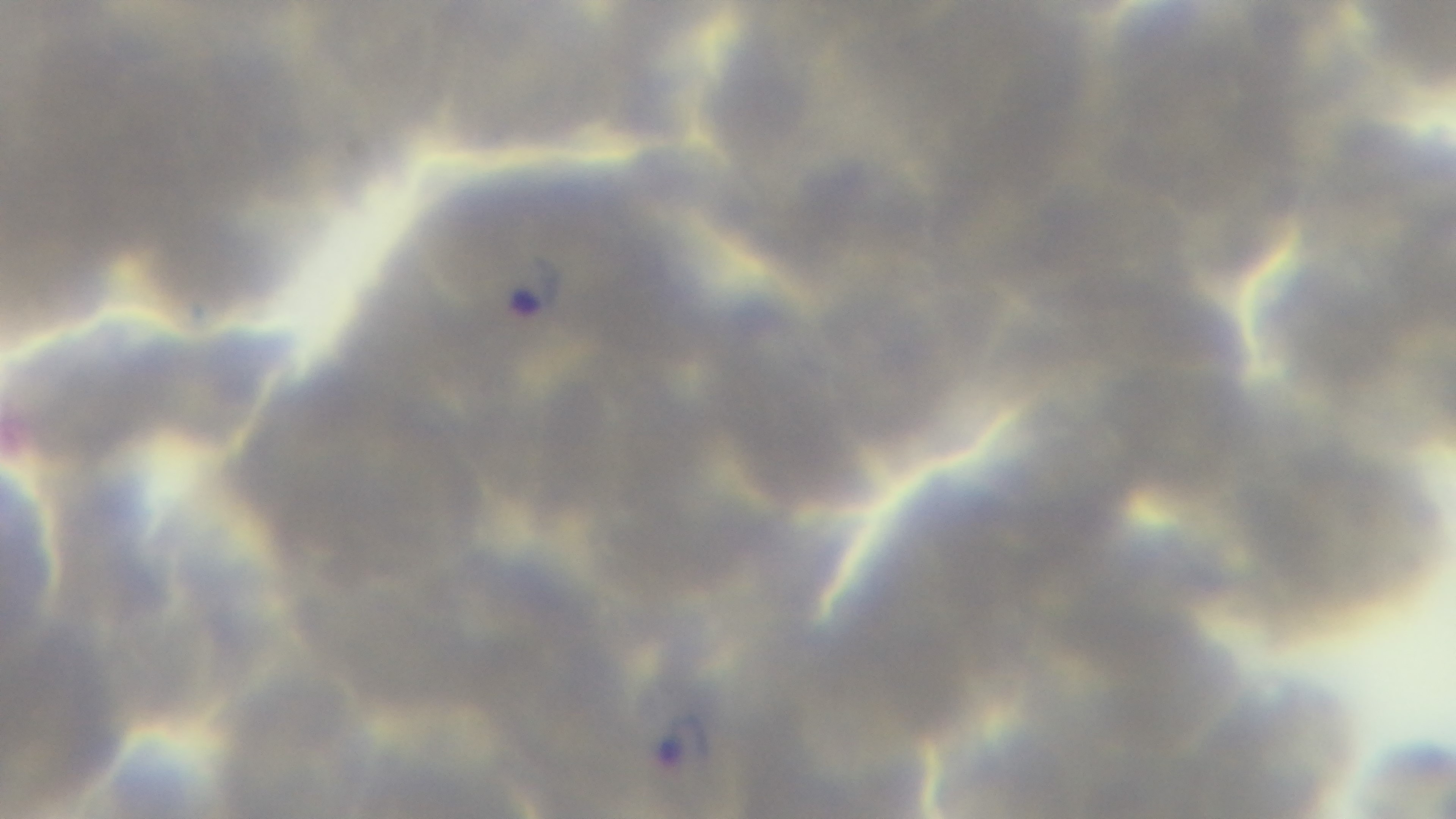
capture = mounted 4K digital camera
stain = Giemsa
malaria status = infected
preparation = thin
field of view = one from the slide
objective = 100x oil immersion
modality = light microscopy